Report the malaria status of this cell.
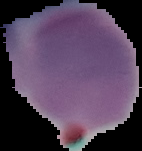

It is uninfected.

preparation = thin blood film
image type = segmented cell region with the area outside set to black
image size = 142×151 pixels